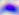
Summary:
  - Modality: photomicrograph
  - Magnification: 400x
  - Identification: Toxoplasma gondii